Locate every Plasmodium vivax-infected red blood cell.
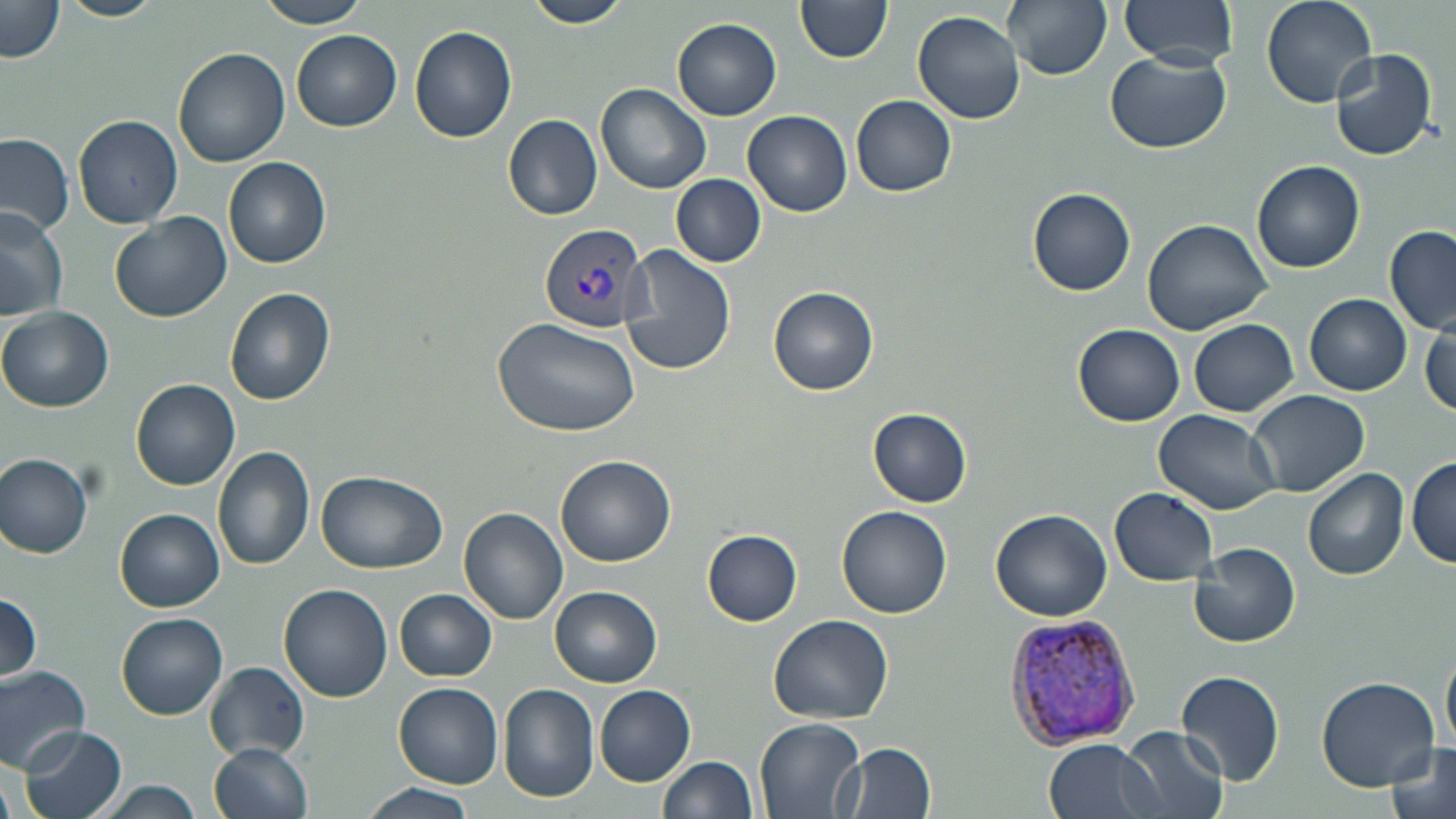
Approximate bounding boxes as (x1, y1, x2, y2) in pixels.
Plasmodium vivax-infected red blood cells: (539, 221, 652, 332), (1004, 612, 1144, 748).

Uninfected red blood cell locations: (58, 0, 167, 22), (255, 0, 373, 28), (521, 0, 630, 28), (795, 0, 894, 63), (1004, 0, 1112, 80), (1120, 0, 1239, 67), (1259, 0, 1376, 107), (2, 2, 65, 64), (913, 10, 1026, 123), (672, 18, 782, 121), (410, 24, 517, 143), (293, 31, 402, 133), (173, 46, 290, 169), (1329, 48, 1438, 163), (1104, 50, 1233, 153), (598, 84, 712, 194), (852, 95, 956, 197), (743, 109, 852, 216), (74, 113, 183, 228), (502, 113, 604, 221), (0, 132, 75, 236), (224, 158, 330, 268), (1250, 159, 1365, 273), (672, 173, 766, 268), (1027, 185, 1136, 297), (0, 203, 70, 323), (108, 212, 233, 324), (1143, 216, 1275, 336), (1384, 224, 1456, 334), (620, 245, 735, 376), (769, 285, 879, 395), (225, 287, 335, 404), (1305, 293, 1412, 395), (1, 307, 113, 413), (494, 317, 642, 437), (1188, 318, 1299, 417), (1419, 318, 1455, 419), (1072, 325, 1185, 427), (131, 379, 240, 490), (1246, 388, 1370, 497), (869, 407, 974, 506), (1154, 409, 1281, 514), (212, 445, 315, 569), (0, 452, 94, 557), (555, 455, 675, 568), (1409, 456, 1456, 569), (1302, 468, 1409, 582), (317, 472, 446, 573), (1109, 487, 1219, 584), (837, 504, 952, 618), (459, 508, 568, 624), (991, 508, 1112, 622), (116, 509, 224, 611), (702, 529, 802, 625), (1191, 543, 1300, 647), (280, 582, 392, 702), (551, 585, 662, 686), (395, 588, 498, 681), (0, 593, 43, 683), (117, 613, 228, 719), (768, 613, 895, 723), (1442, 636, 1456, 758), (206, 661, 307, 756), (0, 665, 92, 772), (1176, 668, 1286, 785), (1315, 676, 1439, 790), (393, 683, 504, 788), (498, 683, 601, 803), (594, 686, 695, 786), (755, 719, 866, 817), (18, 725, 128, 819), (1120, 727, 1230, 819), (1043, 739, 1160, 819), (1382, 741, 1455, 819), (208, 742, 313, 819), (840, 743, 936, 819), (661, 756, 757, 819), (90, 779, 208, 818), (358, 781, 480, 819). Slide-level diagnosis: Plasmodium vivax. Thin blood smear. 1000x magnification. Light microscopy. Single field of view. Image is 1456×819 pixels. May-Grünwald-Giemsa stain.